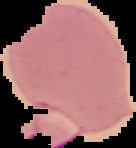

Image is 136×148 pixels. Result: Plasmodium parasites detected. The area outside the segmented cell region is set to black. From a thin blood film.